Identify the parasite.
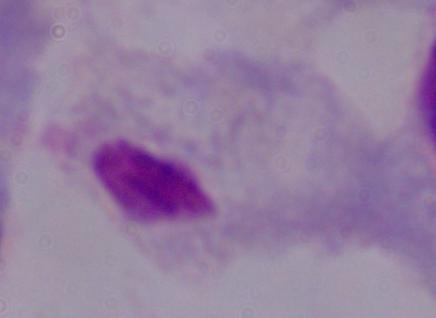
This is a trichomonad.

modality = photomicrograph
magnification = 1000x